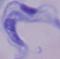
1000x magnification. Micrograph. A trypanosome is shown.